Outline each blood parasite and name the species.
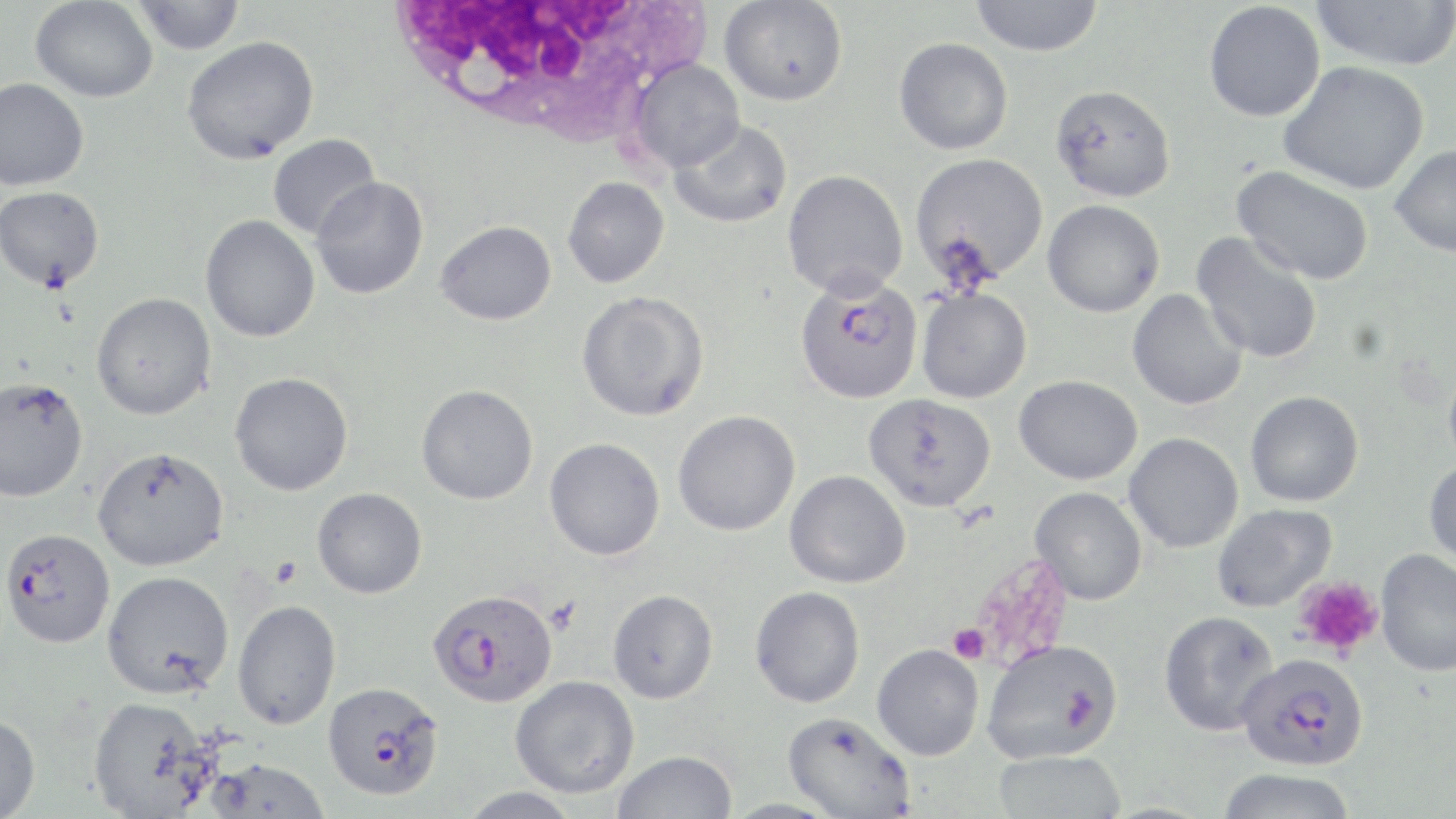

Approximate bounding boxes as (x1, y1, x2, y2) in pixels.
Plasmodium falciparum-infected red blood cells: (794, 275, 923, 404), (1, 528, 115, 648), (427, 587, 558, 707), (1236, 653, 1369, 771), (322, 682, 444, 801).
No Plasmodium ovale, Plasmodium malariae, Plasmodium vivax, Babesia divergens, or Trypanosoma brucei observed.

Platelet locations: (269, 555, 304, 589), (1293, 576, 1383, 659), (948, 623, 989, 664). Uninfected red blood cell locations: (31, 0, 158, 102), (131, 0, 246, 54), (719, 0, 848, 106), (969, 0, 1104, 57), (1311, 1, 1455, 71), (1203, 2, 1325, 122), (181, 36, 319, 164), (893, 37, 1013, 155), (630, 58, 745, 171), (1278, 61, 1430, 195), (0, 78, 90, 190), (1050, 83, 1177, 203), (670, 118, 793, 229), (267, 134, 381, 240), (1389, 144, 1456, 258), (909, 153, 1049, 287), (1233, 166, 1374, 284), (782, 169, 908, 299), (562, 176, 669, 288), (311, 177, 428, 299), (0, 185, 104, 291), (1042, 199, 1165, 317), (200, 214, 320, 342), (436, 220, 556, 325), (1191, 232, 1324, 364), (916, 287, 1033, 404), (1127, 289, 1247, 410), (575, 290, 710, 422), (91, 292, 216, 420), (1443, 361, 1456, 476), (229, 372, 353, 496), (1014, 375, 1143, 485), (0, 376, 88, 502), (416, 384, 539, 505), (1245, 391, 1364, 507), (864, 393, 997, 512), (673, 410, 800, 536), (1124, 432, 1243, 553), (544, 437, 665, 560), (92, 446, 229, 571), (1424, 458, 1456, 569), (784, 470, 911, 589), (312, 487, 427, 599), (1029, 487, 1147, 604), (1211, 504, 1336, 613), (1376, 549, 1456, 676), (102, 570, 233, 698), (750, 586, 865, 708), (607, 589, 718, 703), (232, 600, 341, 730), (1160, 610, 1279, 736), (982, 638, 1124, 763), (872, 644, 984, 760), (510, 676, 640, 798), (88, 695, 213, 817), (782, 711, 915, 818), (0, 713, 40, 819), (611, 749, 737, 819), (992, 749, 1127, 819), (203, 758, 330, 818), (1214, 768, 1358, 819), (457, 787, 584, 819), (720, 797, 845, 818). White blood cell locations: (381, 2, 711, 139). Slide-level diagnosis: Plasmodium falciparum. Single field of view. Image is 1456×819 pixels. Light microscopy. May-Grünwald-Giemsa-stained preparation. Captured at 1000x magnification. Thin blood smear.